Assess this cell for malaria.
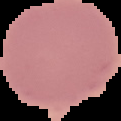

It is uninfected.

From a thin blood film. Image is 121×121 pixels. Cell region segmented out of the field of view; the surrounding area is masked to black.